Classify this cell by malaria status.
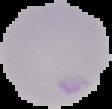

Uninfected.

Summary:
  - Image type: cell region segmented out of the field of view; surrounding area masked to black
  - Image size: 112×109 pixels
  - Preparation: thin blood smear